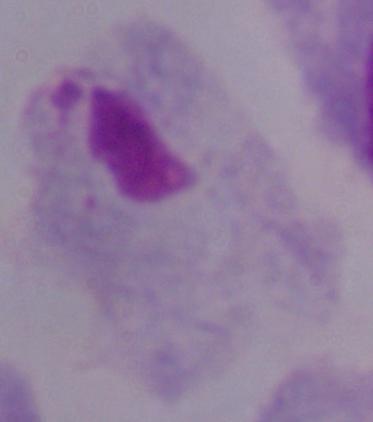
identification = trichomonad
modality = micrograph
magnification = 1000x